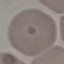
malaria status = uninfected
image type = cell patch, automatically extracted from a larger field of view and resized to 64 × 64 pixels
preparation = thin blood film
capture = smartphone camera at the microscope eyepiece
stain = Giemsa